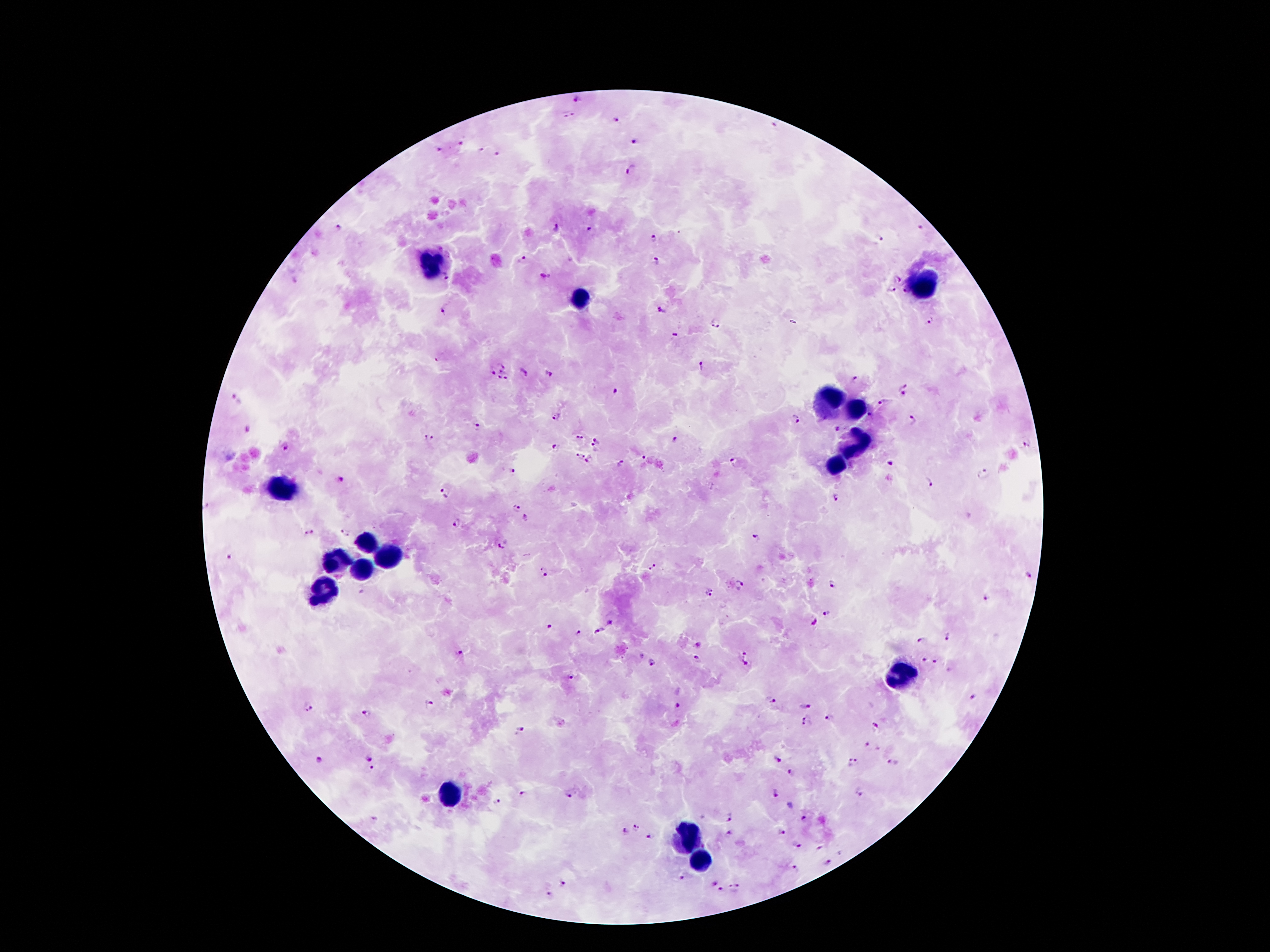
Approximate centers as {x, y} in pixels.
Summary:
  - Leukocyte locations: {429, 266}, {925, 287}, {582, 299}, {830, 402}, {851, 411}, {855, 442}, {839, 467}, {282, 490}, {366, 543}, {389, 556}, {335, 561}, {362, 570}, {322, 593}, {900, 675}, {447, 793}, {686, 836}, {702, 860}
  - Plasmodium parasite locations: {577, 98}, {569, 116}, {617, 122}, {776, 127}, {634, 140}, {461, 143}, {439, 150}, {480, 150}, {497, 153}, {631, 169}, {338, 226}, {556, 228}, {922, 229}, {591, 230}, {653, 238}, {880, 239}, {524, 259}, {655, 261}, {546, 277}, {446, 279}, {898, 279}, {893, 289}, {904, 291}, {445, 309}, {661, 309}, {930, 318}, {715, 324}, {674, 334}, {502, 361}, {701, 365}, {490, 370}, {523, 371}, {500, 372}, {550, 373}, {507, 377}, {500, 379}, {855, 381}, {901, 385}, {616, 390}, {903, 394}, {235, 400}, {884, 402}, {871, 414}, {556, 416}, {796, 418}, {913, 420}, {478, 427}, {837, 429}, {428, 437}, {579, 438}, {676, 439}, {598, 441}, {1027, 442}, {285, 446}, {556, 447}, {594, 449}, {584, 454}, {644, 458}, {578, 460}, {590, 461}, {736, 461}, {621, 463}, {891, 463}, {514, 471}, {985, 473}, {340, 480}, {929, 482}, {443, 492}, {835, 498}, {518, 509}, {526, 518}, {458, 523}, {310, 533}, {345, 533}, {757, 536}, {500, 546}, {229, 557}, {652, 567}, {543, 572}, {1029, 575}, {832, 584}, {741, 585}, {711, 592}, {985, 598}, {826, 612}, {815, 623}, {610, 624}, {548, 626}, {576, 630}, {598, 630}, {947, 637}, {922, 640}, {698, 645}, {744, 652}, {460, 656}, {925, 659}, {697, 660}, {937, 661}, {652, 662}, {744, 664}, {572, 678}, {973, 697}, {774, 700}, {430, 704}, {677, 705}, {309, 706}, {807, 706}, {367, 715}, {807, 717}, {830, 717}, {806, 726}, {875, 728}, {520, 730}, {868, 745}, {369, 758}, {777, 760}, {320, 762}, {855, 763}, {893, 763}, {373, 769}, {791, 773}, {860, 792}, {776, 793}, {569, 794}, {522, 795}, {498, 803}, {732, 815}, {806, 820}, {636, 827}, {625, 830}, {782, 831}, {731, 832}, {652, 836}, {799, 844}, {818, 848}, {829, 863}, {796, 869}, {684, 877}, {713, 883}, {565, 884}, {720, 889}, {733, 889}, {551, 895}
  - Field of view: single
  - Stain: Giemsa
  - Capture: smartphone camera through the microscope eyepiece
  - Image size: 1270×952 pixels
  - Magnification: 100x
  - Preparation: thick blood film
  - Patient malaria status: positive for Plasmodium falciparum